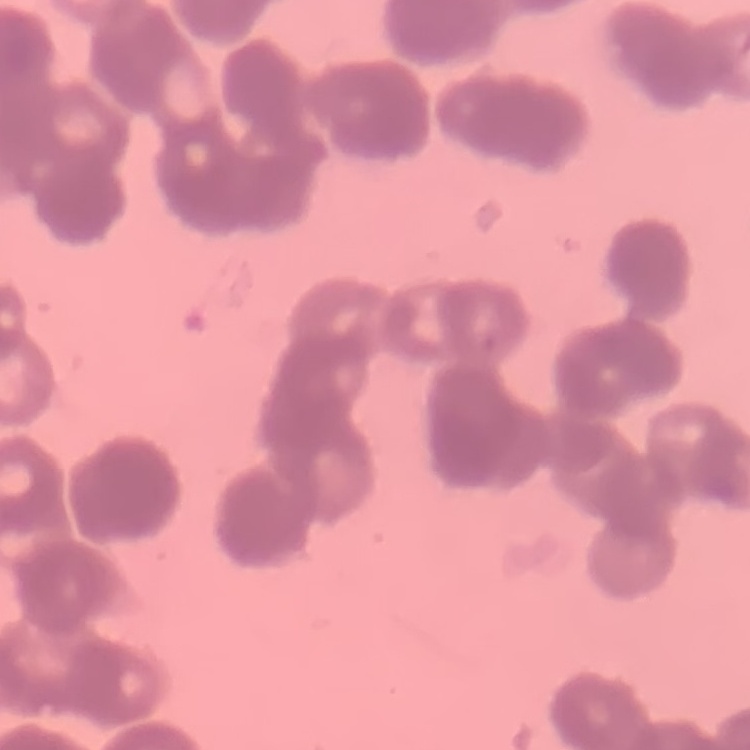

The erythrocytes exhibit rouleaux formation. Square crop of a larger photomicrograph. Field's or Giemsa stain. Thin blood film.